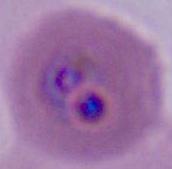

modality = photomicrograph
magnification = 400x or 1000x
identification = Plasmodium